Outline each Plasmodium ovale-infected red blood cell.
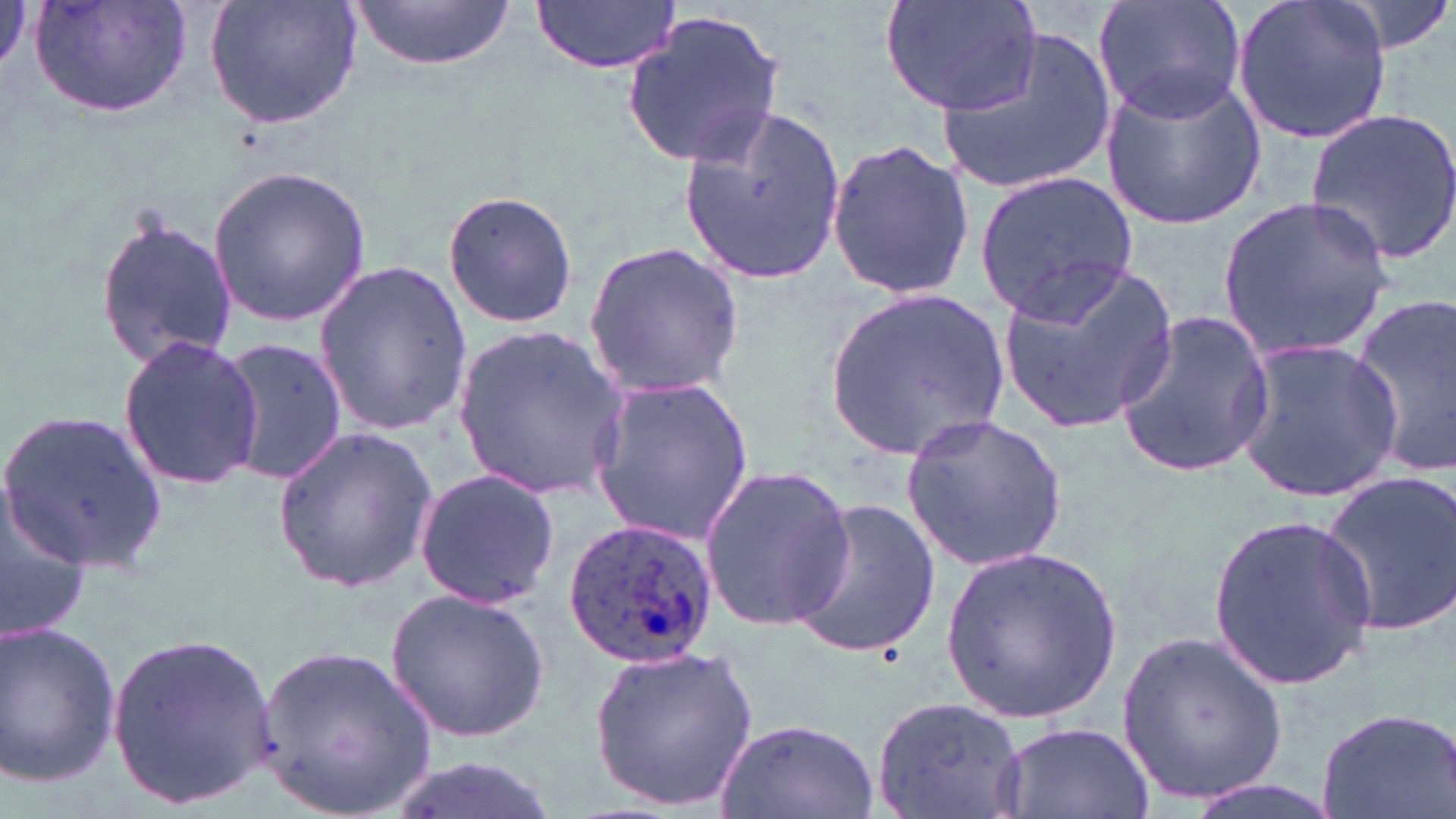
Approximate bounding boxes as [x1, y1, x2, y2] in pixels.
Plasmodium ovale-infected red blood cells: [560, 515, 721, 669].

Uninfected red blood cell locations: [0, 0, 30, 84], [30, 0, 194, 123], [204, 0, 363, 132], [881, 0, 1043, 117], [1093, 0, 1247, 124], [1232, 0, 1393, 146], [1328, 0, 1455, 60], [532, 1, 683, 74], [350, 2, 517, 72], [621, 11, 787, 170], [935, 30, 1119, 199], [1098, 69, 1264, 231], [681, 102, 846, 285], [1304, 107, 1456, 262], [825, 139, 976, 302], [207, 164, 373, 328], [976, 170, 1138, 322], [442, 191, 579, 329], [1216, 193, 1394, 362], [95, 210, 236, 372], [582, 238, 748, 402], [996, 261, 1179, 435], [311, 264, 476, 434], [827, 285, 1010, 456], [1348, 290, 1456, 482], [1113, 310, 1276, 480], [450, 323, 628, 505], [117, 334, 265, 490], [218, 336, 346, 486], [1233, 336, 1405, 499], [587, 376, 754, 546], [1, 411, 167, 571], [902, 412, 1066, 573], [271, 427, 441, 592], [700, 465, 854, 630], [413, 468, 560, 610], [1316, 468, 1456, 639], [0, 487, 90, 647], [784, 500, 942, 661], [1206, 512, 1377, 689], [941, 544, 1121, 718], [386, 587, 551, 744], [0, 619, 122, 790], [1119, 630, 1288, 808], [107, 631, 276, 809], [256, 645, 435, 815], [589, 645, 758, 812], [870, 693, 1032, 819], [1314, 706, 1454, 819], [713, 718, 882, 818], [993, 721, 1156, 819], [382, 755, 560, 819], [1178, 773, 1346, 819]. Slide-level diagnosis: Plasmodium ovale. Optical microscopy. Thin blood smear. Image is 1456×819 pixels. May-Grünwald-Giemsa stain. One field of a larger specimen. 1000x magnification.